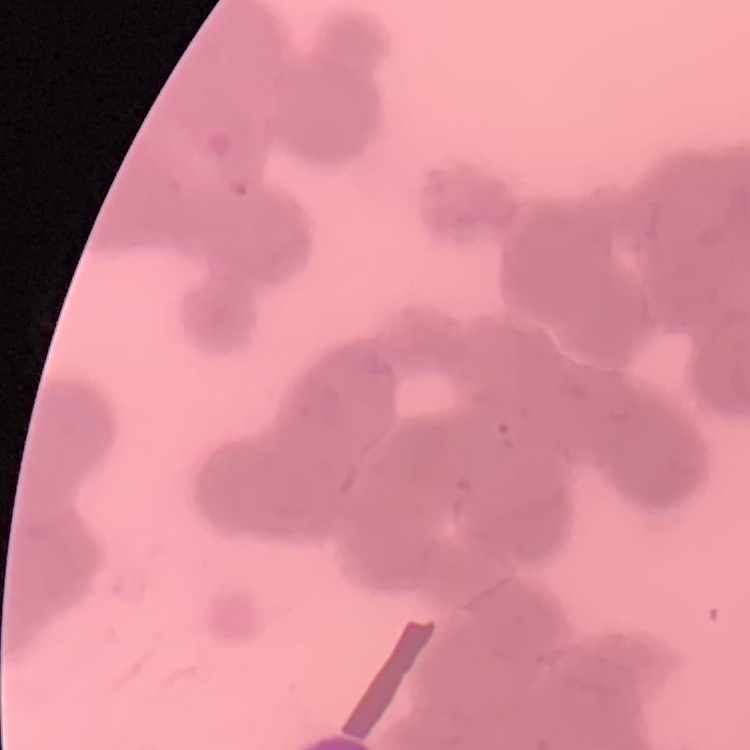 The red blood cells show rouleaux formation. Field's or Giemsa stain. Square crop of a larger photomicrograph. Thin blood film.